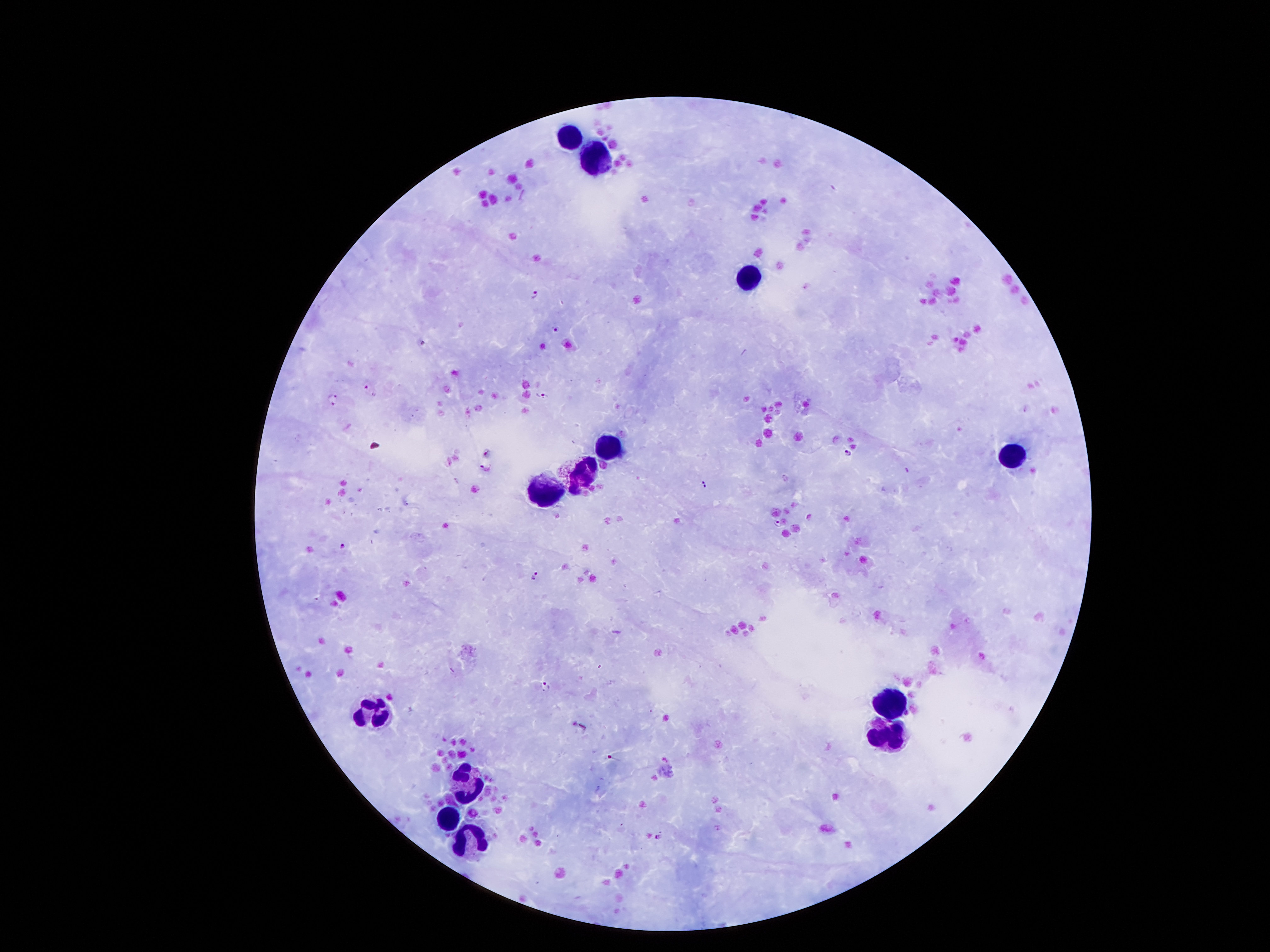

Approximate centers as {x, y} in pixels. Malaria parasite locations: {536, 294}, {556, 329}, {367, 385}, {542, 394}, {334, 400}, {848, 452}, {485, 467}, {778, 524}, {343, 545}, {536, 577}, {545, 685}, {581, 727}, {658, 837}. Leukocyte locations: {571, 135}, {598, 163}, {746, 279}, {609, 445}, {1016, 459}, {582, 474}, {546, 492}, {893, 701}, {366, 717}, {884, 740}, {464, 782}, {453, 817}, {464, 844}. Image is 1270×952 pixels. Giemsa-stained preparation. Thick blood film. Patient malaria status: positive for Plasmodium falciparum. Single field of view. Smartphone photograph taken through the microscope eyepiece. 100x magnification.